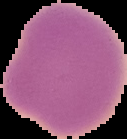
image size = 127×139 pixels
image type = cell region segmented out of the field of view; surrounding area masked to black
preparation = thin blood film
result = no Plasmodium parasites detected